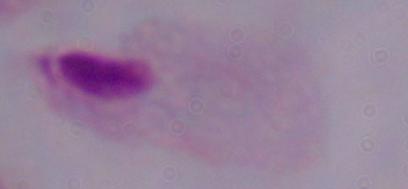

Summary:
  - Identification: trichomonad
  - Magnification: 1000x
  - Modality: micrograph